Locate every blood parasite and identify its species.
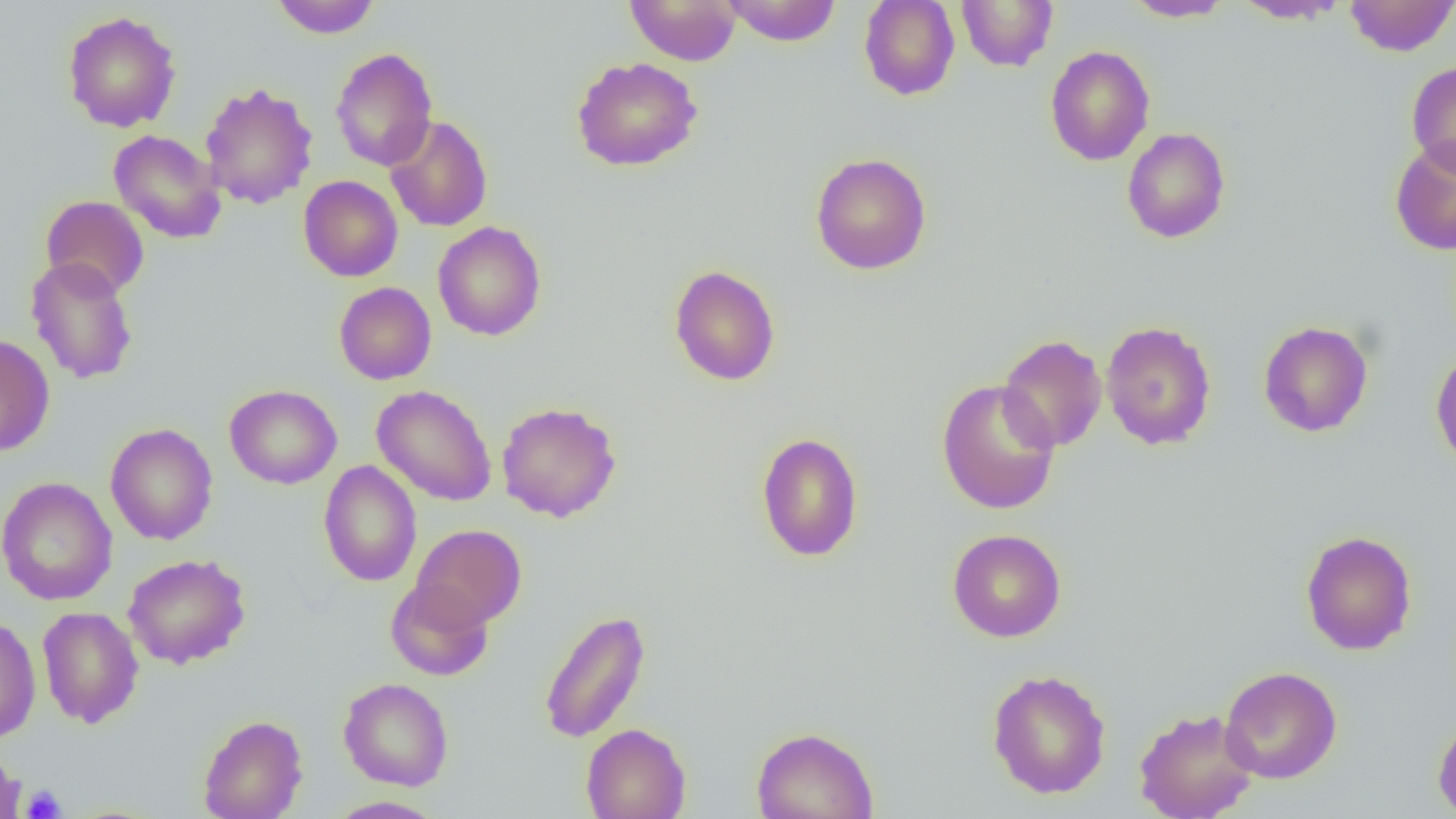
No blood parasites observed.

slide_level_diagnosis: no evidence of blood parasites
field_of_view: single
modality: light microscopy
uninfected_red_blood_cell_locations: 'approximate bounding boxes as (x1, y1, x2, y2) in pixels: (271, 0, 382, 38), (625, 0, 741, 65), (721, 0, 842, 46), (858, 0, 960, 101), (957, 0, 1059, 72), (1124, 0, 1235, 22), (1232, 0, 1350, 24), (1344, 0, 1456, 56), (62, 10, 182, 133), (1044, 46, 1155, 166), (330, 47, 438, 172), (570, 56, 703, 172), (1406, 61, 1456, 175), (199, 82, 319, 209), (384, 115, 493, 232), (1122, 127, 1231, 244), (108, 129, 227, 244), (1389, 137, 1456, 255), (810, 152, 932, 275), (298, 175, 403, 282), (40, 195, 149, 299), (432, 221, 547, 341), (25, 255, 139, 386), (669, 264, 780, 386), (334, 282, 436, 385), (1101, 320, 1217, 451), (1258, 320, 1373, 437), (0, 334, 55, 457), (997, 334, 1108, 452), (1431, 348, 1456, 472), (936, 378, 1061, 515), (224, 384, 342, 489), (372, 385, 497, 507), (496, 401, 622, 523), (105, 423, 218, 545), (755, 431, 864, 562), (318, 460, 422, 587), (0, 476, 118, 606), (411, 524, 526, 629), (947, 528, 1067, 642), (1299, 530, 1417, 655), (122, 553, 251, 669), (385, 578, 494, 681), (36, 606, 144, 728), (538, 608, 651, 744), (0, 614, 41, 744), (1220, 666, 1341, 784), (987, 669, 1111, 799), (338, 677, 454, 791), (1134, 707, 1259, 819), (198, 714, 307, 819), (1432, 715, 1456, 818), (580, 723, 691, 819), (750, 726, 879, 819), (0, 750, 25, 819), (326, 795, 445, 818)'
magnification: 1000x
preparation: thin blood smear
image_size: 1456×819 pixels
platelet_locations: 'approximate bounding boxes as (x1, y1, x2, y2) in pixels: (20, 784, 67, 819)'